Identify the parasite.
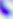

This is Toxoplasma gondii.

modality: micrograph
magnification: 400x